Report the malaria status of this cell.
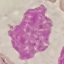

Uninfected.

Giemsa-stained preparation. Cell patch, automatically extracted from a larger field of view and resized to 64 × 64 pixels. Photographed with a smartphone camera at the microscope eyepiece. Thin smear of blood.